Locate every malaria parasite.
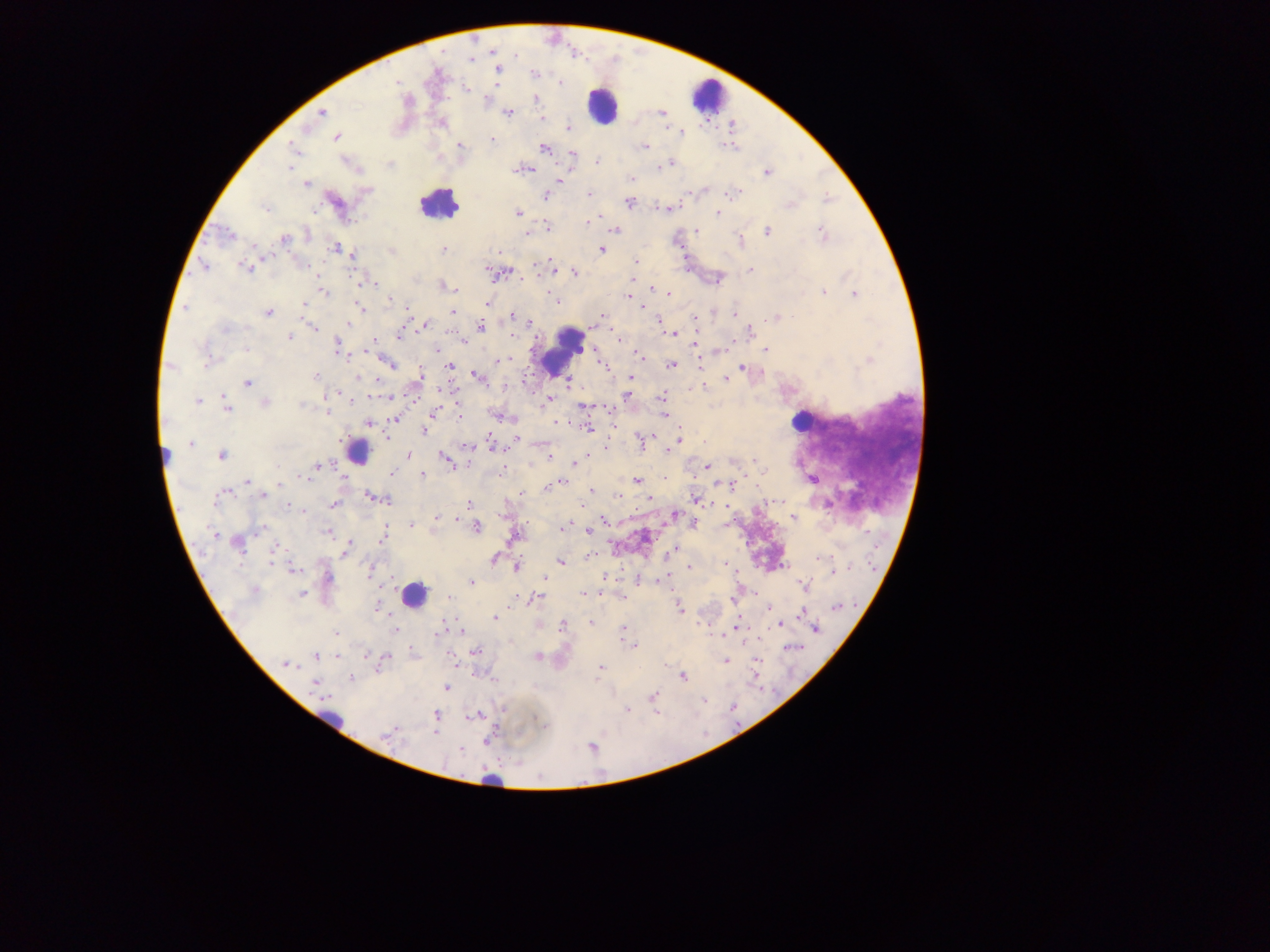

Approximate centers as (x, y) in pixels.
Malaria parasites: (472, 59), (497, 70), (535, 75), (560, 82), (494, 83), (468, 91), (534, 100), (321, 113), (508, 113), (660, 116), (543, 117), (441, 121), (568, 127), (681, 133), (335, 135), (493, 139), (460, 145), (644, 147), (544, 148), (731, 148), (294, 152), (572, 154), (598, 160), (672, 161), (392, 163), (289, 169), (528, 170), (767, 170), (559, 179), (628, 179), (630, 180), (305, 184), (732, 193), (589, 194), (544, 195), (827, 200), (628, 203), (671, 208), (266, 210), (517, 213), (716, 213), (592, 221), (588, 223), (821, 225), (546, 226), (615, 231), (767, 231), (225, 233), (528, 233), (696, 233), (283, 239), (740, 240), (336, 248), (444, 249), (601, 250), (353, 257), (270, 258), (635, 261), (552, 263), (244, 266), (204, 269), (749, 269), (493, 273), (575, 273), (319, 275), (632, 280), (368, 283), (654, 289), (456, 290), (822, 291), (324, 292), (668, 294), (852, 294), (554, 298), (392, 299), (634, 299), (557, 300), (488, 304), (304, 306), (185, 307), (642, 307), (183, 309), (361, 309), (453, 312), (734, 312), (268, 313), (511, 315), (601, 315), (777, 317), (694, 319), (528, 323), (348, 324), (696, 324), (424, 325), (226, 328), (312, 329), (481, 329), (749, 332), (669, 333), (674, 335), (398, 336), (514, 337), (619, 337), (290, 338), (694, 343), (338, 344), (581, 348), (247, 349), (436, 351), (721, 351), (766, 352), (639, 356), (869, 359), (390, 363), (671, 365), (448, 367), (606, 367), (173, 368), (743, 368), (315, 376), (475, 376), (630, 376), (359, 378), (421, 378), (725, 378), (568, 381), (249, 384), (701, 387), (444, 390), (336, 394), (625, 394), (388, 397), (662, 397), (549, 401), (197, 402), (229, 405), (266, 405), (302, 405), (583, 407), (228, 408), (327, 411), (431, 414), (665, 415), (395, 418), (459, 418), (555, 421), (368, 424), (586, 427), (424, 431), (678, 438), (388, 441), (514, 442), (191, 444), (638, 444), (467, 448), (671, 448), (668, 450), (222, 456), (408, 456), (550, 456), (445, 458), (755, 459), (578, 462), (448, 463), (575, 464), (319, 465), (706, 465), (763, 470), (393, 472), (422, 474), (636, 480), (246, 481), (282, 482), (561, 482), (735, 486), (545, 488), (589, 490), (222, 492), (226, 492), (692, 494), (263, 496), (617, 496), (369, 498), (695, 498), (387, 500), (648, 501), (469, 503), (334, 505), (289, 506), (721, 506), (676, 512), (304, 513), (435, 519), (457, 519), (604, 520), (695, 524), (412, 525), (478, 527), (564, 527), (258, 528), (560, 528), (587, 532), (327, 533), (214, 534), (384, 537), (380, 540), (239, 547), (273, 550), (674, 551), (345, 552), (588, 556), (819, 559), (495, 560), (560, 563), (272, 564), (725, 564), (516, 567), (688, 567), (291, 570), (369, 573), (833, 574), (543, 578), (470, 582), (472, 584), (803, 587), (302, 593), (583, 593), (446, 597), (539, 597), (678, 603), (376, 604), (768, 607), (835, 607), (680, 609), (802, 612), (493, 617), (590, 621), (561, 623), (778, 625), (558, 626), (622, 629), (393, 630), (816, 630), (461, 631), (336, 632), (439, 634), (722, 636), (629, 647), (635, 647), (475, 651), (316, 655), (537, 656), (386, 658), (757, 661), (724, 662), (285, 664), (454, 665), (755, 665), (601, 668), (682, 677), (353, 680), (313, 683), (653, 696), (703, 700), (435, 735).

preparation = thick blood smear
image size = 1270×952 pixels
country = Ghana
field of view = single
capture = mobile-phone photograph through a microscope
leukocyte locations = approximate centers as (x, y) in pixels: (708, 96), (598, 108), (432, 208), (562, 351), (803, 419), (355, 450), (412, 599)